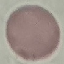
Result: no malaria parasites seen. Automatically extracted cell patch, resized to 64 × 64 pixels. Giemsa-stained preparation. Acquired by smartphone through the microscope eyepiece. Thin blood film.